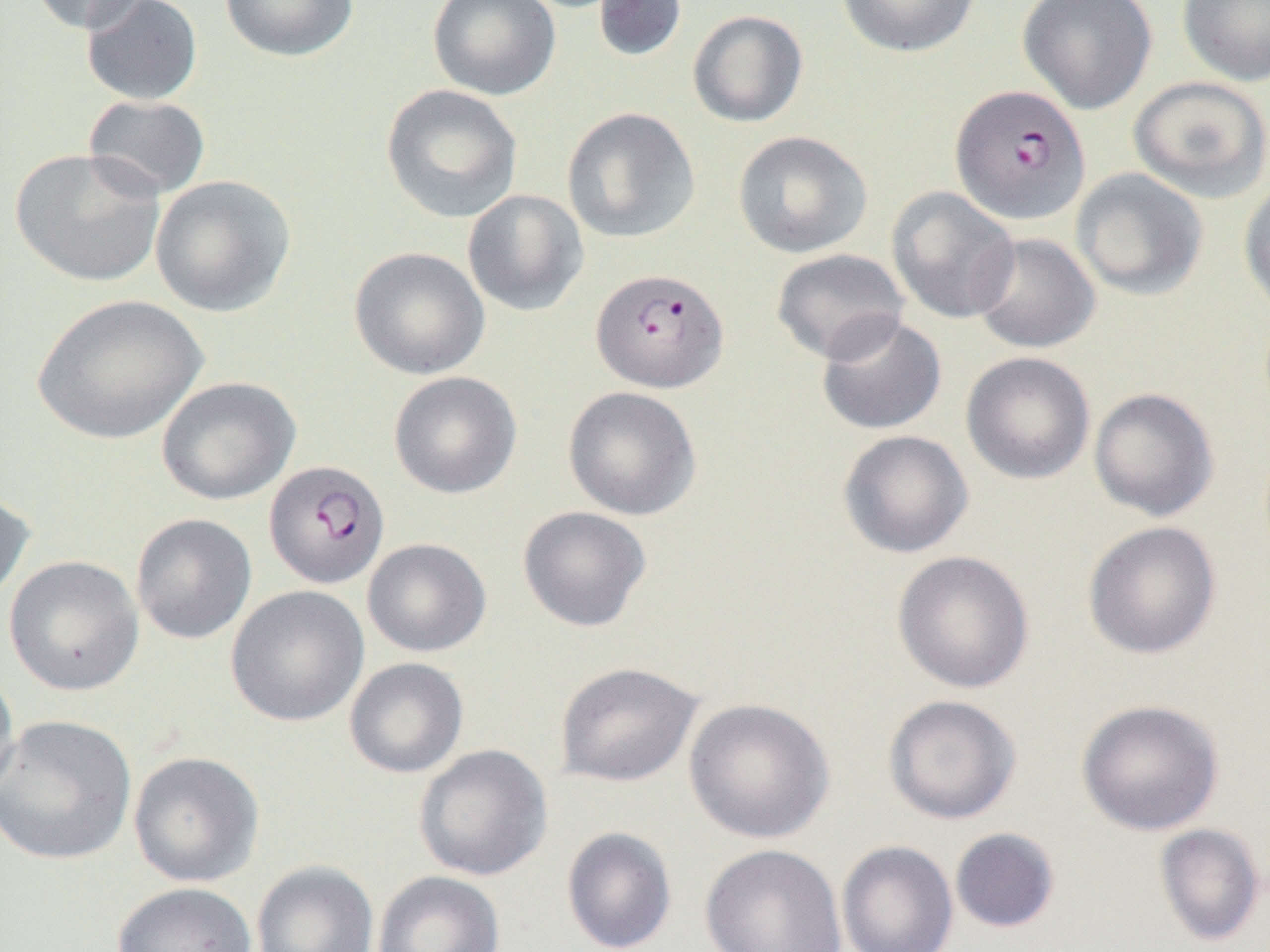

Summary:
  - Coordinate format: approximate bounding boxes as [x1, y1, x2, y2] in pixels
  - Uninfected red blood cell locations: [29, 0, 153, 34], [81, 0, 204, 106], [219, 0, 358, 62], [426, 0, 561, 101], [594, 0, 688, 62], [836, 0, 982, 58], [1017, 0, 1158, 115], [1177, 0, 1270, 86], [687, 9, 809, 128], [1128, 75, 1270, 203], [380, 84, 523, 224], [83, 95, 211, 200], [561, 107, 701, 244], [732, 130, 872, 258], [9, 148, 166, 287], [1070, 168, 1208, 300], [150, 174, 296, 318], [1238, 176, 1270, 321], [886, 186, 1020, 324], [462, 189, 589, 316], [970, 232, 1100, 353], [349, 246, 490, 380], [770, 248, 910, 364], [32, 294, 208, 445], [815, 314, 947, 435], [960, 351, 1095, 484], [389, 371, 522, 499], [156, 376, 300, 505], [562, 386, 702, 520], [1088, 387, 1220, 522], [837, 430, 974, 559], [0, 486, 35, 608], [517, 505, 652, 632], [130, 513, 257, 644], [1082, 521, 1222, 660], [362, 538, 492, 657], [891, 550, 1035, 694], [4, 555, 144, 696], [226, 585, 369, 727], [344, 657, 469, 778], [554, 661, 703, 787], [0, 664, 20, 806], [883, 694, 1022, 824], [683, 697, 835, 844], [1076, 698, 1225, 836], [0, 714, 137, 866], [413, 743, 552, 881], [128, 751, 264, 887], [1154, 823, 1265, 946], [561, 827, 677, 952], [949, 827, 1061, 934], [836, 840, 959, 952], [699, 843, 847, 952], [251, 859, 379, 952], [372, 870, 506, 952], [112, 881, 257, 952]
  - Plasmodium falciparum-infected red blood cell locations: [950, 85, 1090, 225], [591, 267, 729, 393], [264, 460, 389, 589]
  - Slide-level diagnosis: Plasmodium falciparum
  - Modality: light microscopy
  - Preparation: thin blood smear
  - Field of view: single
  - Image size: 1270×952 pixels
  - Magnification: 1000x